Locate every blood parasite and identify its species.
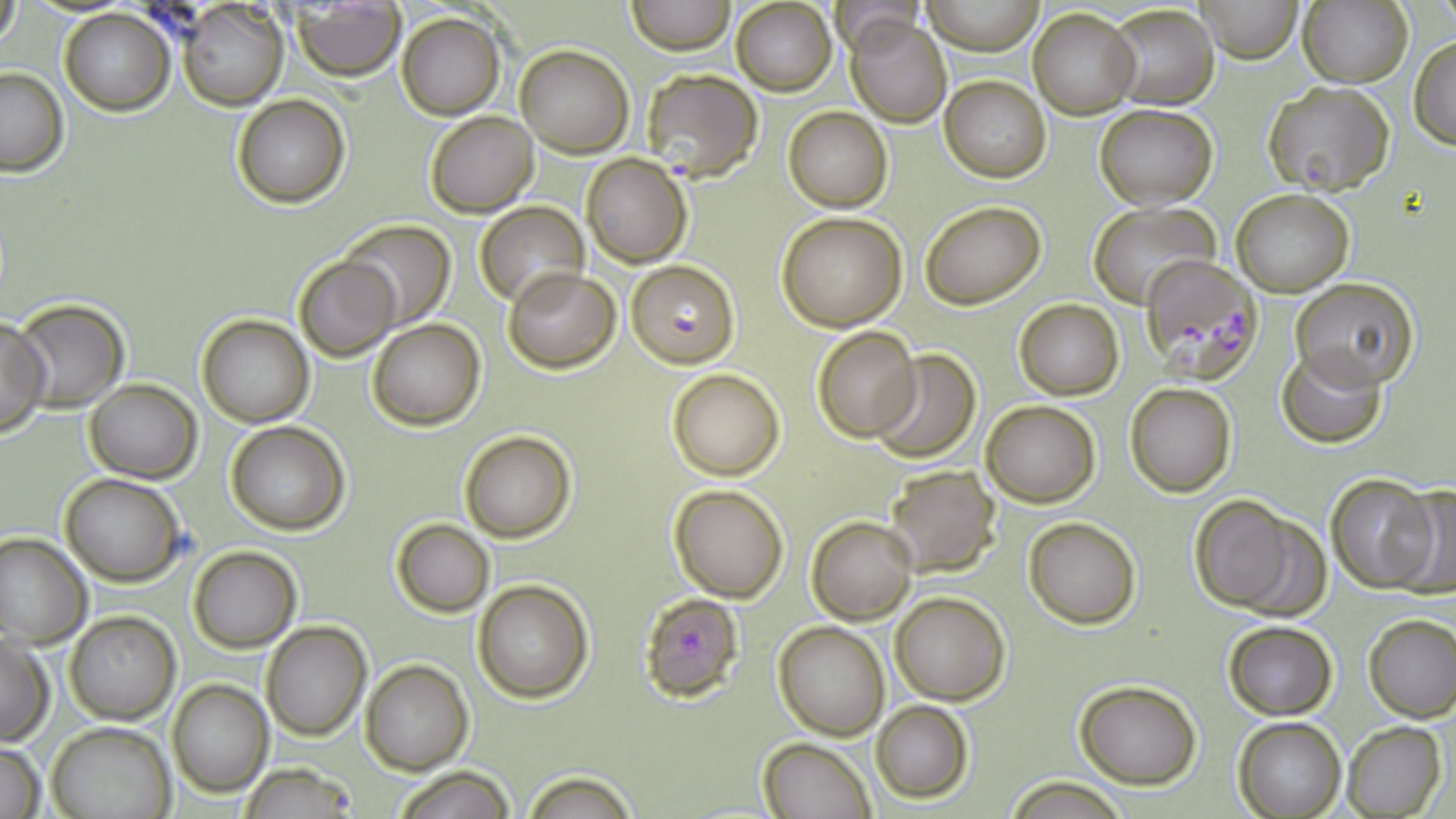
Approximate bounding boxes as (x1, y1, x2, y2) in pixels.
Plasmodium falciparum-infected red blood cells: (639, 67, 762, 183), (1140, 253, 1264, 377), (627, 260, 738, 366), (638, 593, 744, 702), (237, 764, 365, 817).
No Plasmodium ovale, Plasmodium malariae, Plasmodium vivax, Babesia divergens, or Trypanosoma brucei observed.

slide_level_diagnosis: Plasmodium falciparum
modality: light microscopy
image_size: 1456×819 pixels
field_of_view: one of a larger specimen
stain: May-Grünwald-Giemsa
magnification: 1000x
preparation: thin blood film
uninfected_red_blood_cell_locations: 'approximate bounding boxes as (x1, y1, x2, y2) in pixels: (1194, 0, 1303, 63), (1300, 0, 1413, 89), (626, 1, 735, 54), (921, 1, 1044, 54), (731, 2, 836, 95), (1, 3, 21, 53), (177, 3, 288, 111), (292, 5, 406, 80), (1108, 5, 1218, 111), (58, 7, 174, 114), (1029, 8, 1139, 117), (396, 11, 506, 120), (846, 15, 952, 127), (1408, 36, 1456, 150), (515, 44, 634, 157), (0, 67, 69, 176), (939, 75, 1050, 183), (1264, 81, 1394, 196), (231, 95, 349, 207), (1095, 104, 1217, 207), (784, 106, 892, 212), (424, 111, 539, 218), (581, 153, 691, 267), (1231, 188, 1355, 295), (920, 201, 1044, 310), (476, 202, 588, 309), (1089, 202, 1220, 309), (776, 211, 908, 331), (339, 220, 455, 329), (294, 254, 401, 362), (504, 266, 621, 373), (1292, 278, 1421, 388), (9, 298, 130, 411), (1014, 298, 1123, 401), (196, 315, 315, 427), (0, 318, 52, 436), (370, 320, 486, 430), (811, 324, 923, 442), (1277, 346, 1388, 449), (868, 350, 982, 463), (666, 368, 785, 480), (84, 379, 200, 483), (1125, 382, 1237, 497), (981, 400, 1101, 508), (225, 421, 349, 535), (460, 430, 576, 543), (882, 464, 1000, 575), (1325, 471, 1442, 594), (60, 472, 184, 585), (669, 484, 789, 602), (1390, 484, 1456, 599), (1187, 495, 1309, 615), (806, 516, 917, 624), (1023, 516, 1141, 628), (391, 518, 496, 617), (0, 532, 91, 647), (187, 545, 302, 653), (472, 579, 593, 703), (891, 592, 1009, 705), (64, 611, 180, 725), (1362, 614, 1456, 721), (1221, 618, 1339, 721), (260, 620, 372, 740), (773, 620, 890, 738), (0, 634, 53, 745), (360, 658, 473, 775), (1072, 678, 1202, 788), (168, 679, 274, 798), (870, 700, 973, 803), (1233, 717, 1346, 818), (47, 720, 176, 819), (1341, 721, 1446, 818), (759, 737, 875, 819), (0, 742, 46, 818), (393, 765, 517, 819), (523, 768, 638, 818), (1005, 777, 1125, 817)'